Report the malaria status of this cell.
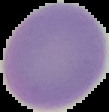
It is uninfected.

preparation = thin blood film
image size = 109×112 pixels
image type = segmented cell region with the area outside set to black